Report the malaria status of this cell.
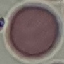

It is uninfected.

preparation = thin blood film
image type = cell patch, automatically extracted from a larger field of view and resized to 64 × 64 pixels
stain = Giemsa
capture = smartphone through the microscope eyepiece